Assess this cell for malaria.
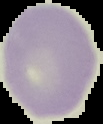
Uninfected.

Segmented cell region on a black background. From a thin blood smear. Image is 103×124 pixels.